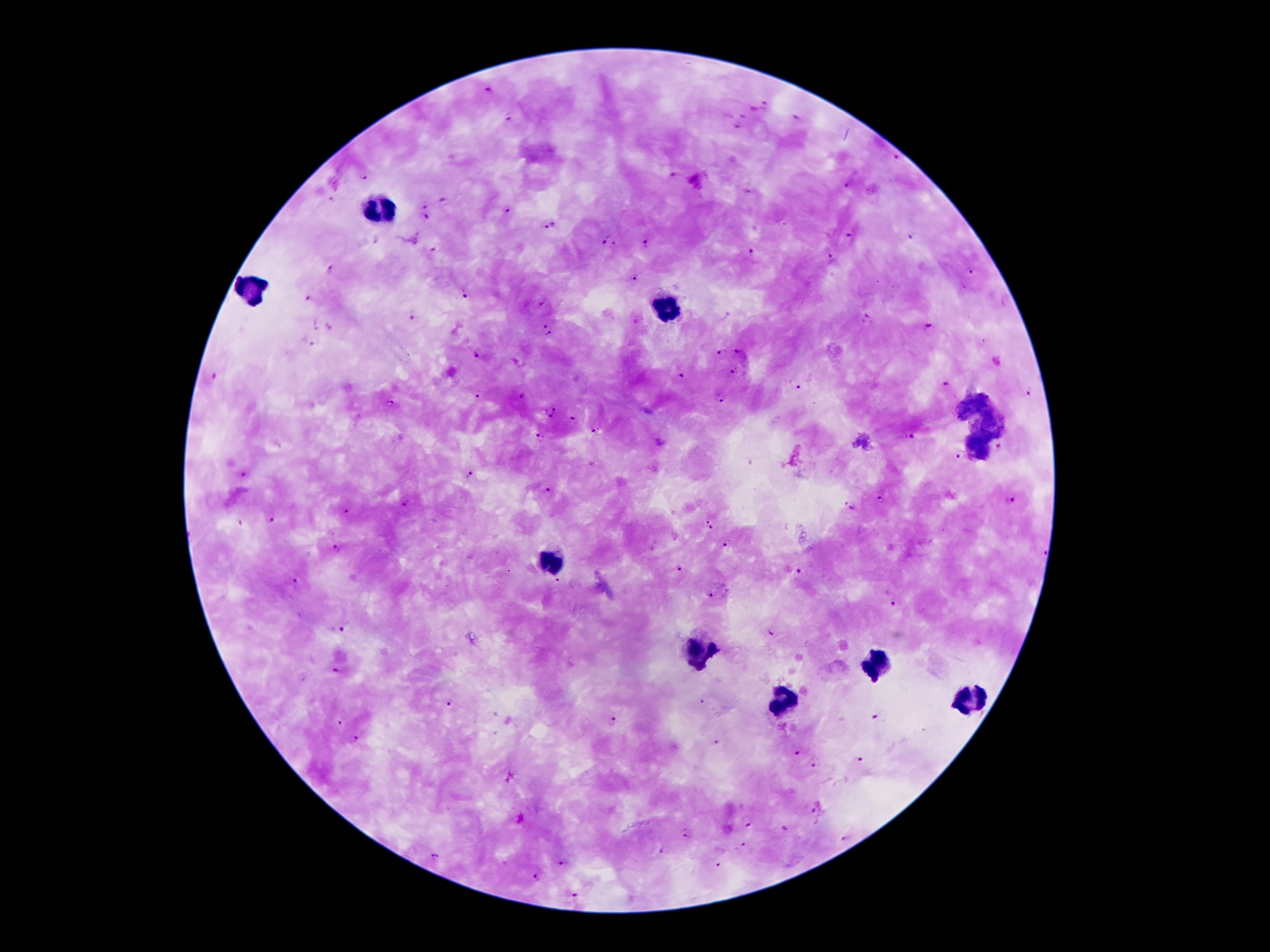
{
  "image_size": "1270×952 pixels",
  "field_of_view": "single",
  "malaria_parasite_locations": "approximate centers as {x, y} in pixels: {488, 89}, {765, 103}, {745, 115}, {510, 117}, {795, 117}, {738, 127}, {895, 157}, {675, 174}, {364, 178}, {847, 184}, {330, 198}, {444, 200}, {424, 205}, {509, 209}, {427, 218}, {551, 227}, {847, 234}, {912, 237}, {607, 238}, {646, 242}, {434, 249}, {752, 250}, {832, 259}, {332, 270}, {970, 272}, {634, 279}, {466, 294}, {307, 301}, {543, 302}, {413, 316}, {868, 319}, {542, 324}, {316, 325}, {332, 325}, {930, 329}, {550, 335}, {312, 342}, {719, 351}, {739, 351}, {474, 356}, {734, 372}, {215, 373}, {681, 373}, {946, 385}, {799, 388}, {1027, 393}, {477, 394}, {521, 396}, {720, 400}, {389, 403}, {549, 410}, {573, 419}, {594, 431}, {911, 438}, {540, 439}, {1000, 446}, {958, 457}, {245, 475}, {468, 475}, {549, 491}, {882, 499}, {1011, 500}, {406, 504}, {850, 507}, {346, 511}, {270, 518}, {241, 524}, {709, 525}, {725, 544}, {337, 549}, {1047, 550}, {681, 567}, {798, 572}, {295, 581}, {557, 582}, {708, 595}, {893, 604}, {342, 630}, {770, 632}, {336, 673}, {701, 700}, {449, 701}, {877, 715}, {613, 720}, {340, 722}, {357, 740}, {717, 740}, {796, 754}, {859, 761}, {814, 764}, {747, 825}, {785, 828}, {686, 835}, {846, 836}, {742, 847}, {658, 852}, {432, 855}, {563, 863}, {536, 878}",
  "magnification": "100x",
  "preparation": "thick blood film",
  "patient_malaria_status": "infected with Plasmodium falciparum",
  "stain": "Giemsa",
  "capture": "smartphone camera through the microscope eyepiece",
  "leukocyte_locations": "approximate centers as {x, y} in pixels: {379, 213}, {253, 289}, {667, 309}, {552, 558}, {699, 646}, {879, 658}, {785, 702}"
}